Identify the cell.
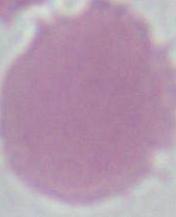
This is an erythrocyte.

Summary:
  - Modality: photomicrograph
  - Magnification: 1000x